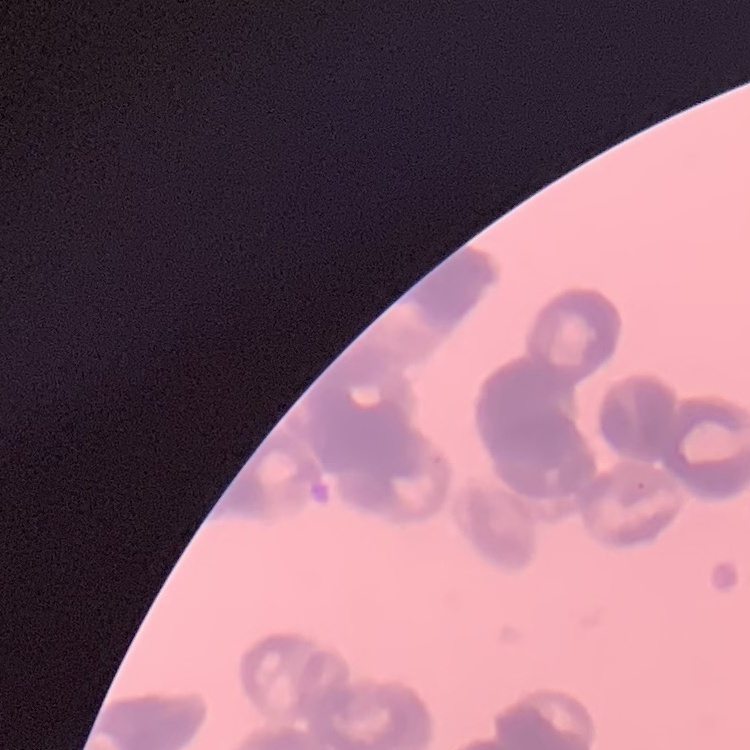

The erythrocytes exhibit rouleaux formation. One tile cut from a larger photomicrograph. Thin blood film. Stained with either Field's or Giemsa.